Locate and identify every blood parasite.
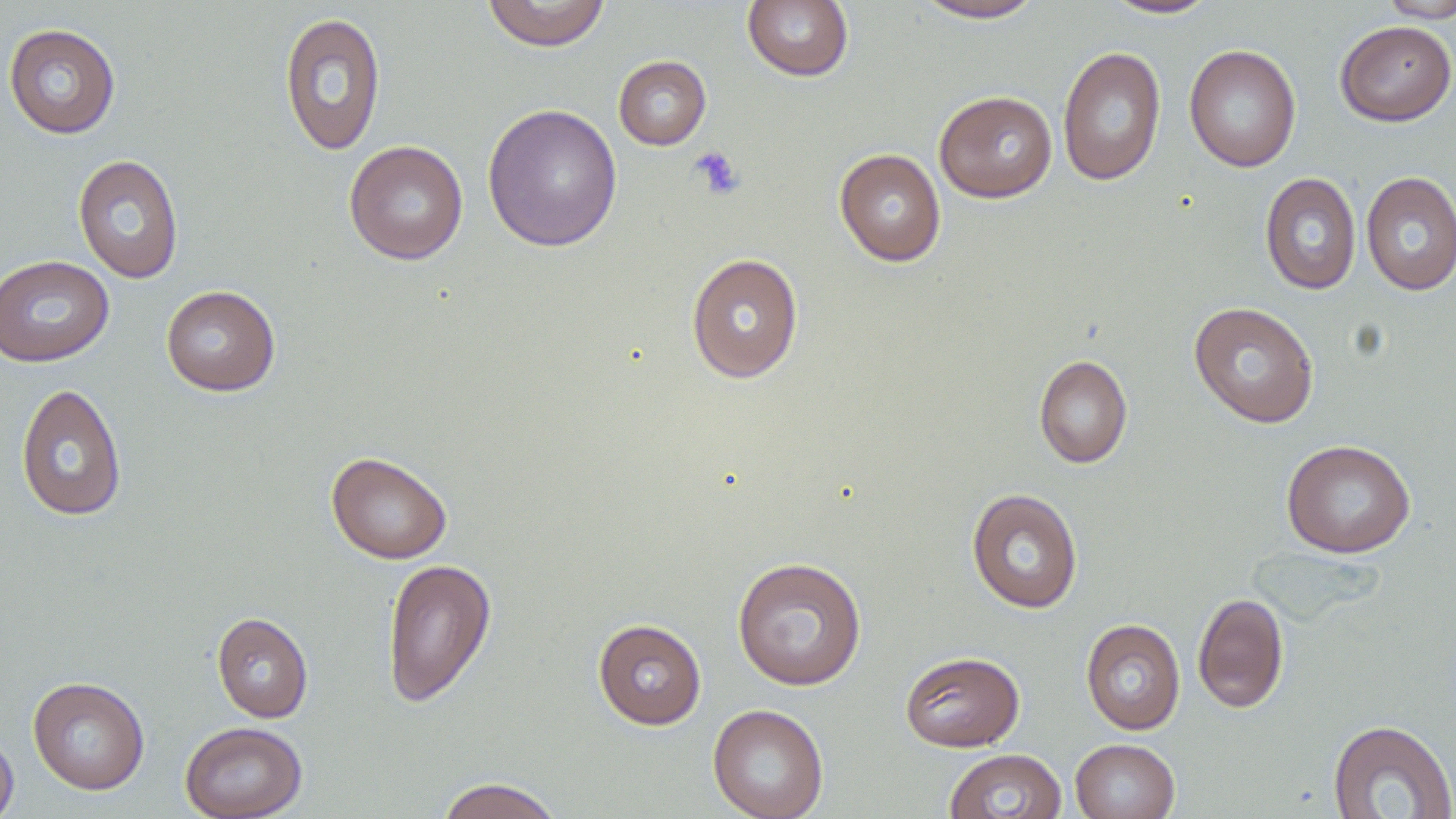
No blood parasites observed.

Approximate bounding boxes as named x1/y1/x2/y2 corners in pixels. Uninfected red blood cell locations: (x1=481, y1=0, x2=612, y2=51), (x1=1102, y1=0, x2=1220, y2=19), (x1=1376, y1=0, x2=1456, y2=23), (x1=741, y1=1, x2=854, y2=82), (x1=912, y1=1, x2=1046, y2=23), (x1=278, y1=11, x2=387, y2=157), (x1=1335, y1=20, x2=1455, y2=126), (x1=3, y1=23, x2=121, y2=139), (x1=1184, y1=44, x2=1301, y2=173), (x1=1057, y1=46, x2=1167, y2=186), (x1=613, y1=55, x2=711, y2=150), (x1=934, y1=90, x2=1058, y2=203), (x1=482, y1=103, x2=623, y2=253), (x1=344, y1=140, x2=469, y2=264), (x1=834, y1=148, x2=946, y2=266), (x1=73, y1=154, x2=184, y2=284), (x1=1361, y1=171, x2=1456, y2=296), (x1=1260, y1=172, x2=1361, y2=295), (x1=685, y1=252, x2=804, y2=384), (x1=0, y1=255, x2=114, y2=367), (x1=161, y1=285, x2=281, y2=396), (x1=1189, y1=301, x2=1320, y2=428), (x1=1033, y1=354, x2=1132, y2=468), (x1=15, y1=383, x2=127, y2=521), (x1=1281, y1=439, x2=1416, y2=558), (x1=326, y1=451, x2=452, y2=564), (x1=966, y1=487, x2=1083, y2=614), (x1=731, y1=556, x2=867, y2=691), (x1=381, y1=557, x2=496, y2=708), (x1=1193, y1=592, x2=1289, y2=713), (x1=212, y1=612, x2=313, y2=723), (x1=1080, y1=618, x2=1186, y2=735), (x1=593, y1=619, x2=707, y2=730), (x1=900, y1=650, x2=1025, y2=752), (x1=27, y1=676, x2=150, y2=795), (x1=707, y1=704, x2=829, y2=819), (x1=1328, y1=718, x2=1456, y2=818), (x1=179, y1=721, x2=308, y2=818), (x1=0, y1=730, x2=19, y2=819), (x1=1070, y1=739, x2=1180, y2=819), (x1=944, y1=749, x2=1067, y2=819), (x1=435, y1=776, x2=564, y2=819). Platelet locations: (x1=690, y1=146, x2=746, y2=199). Slide-level diagnosis: no evidence of blood parasites. Single field of view. 1000x magnification. May-Grünwald-Giemsa stain. Light microscopy. Thin blood film. Image is 1456×819 pixels.